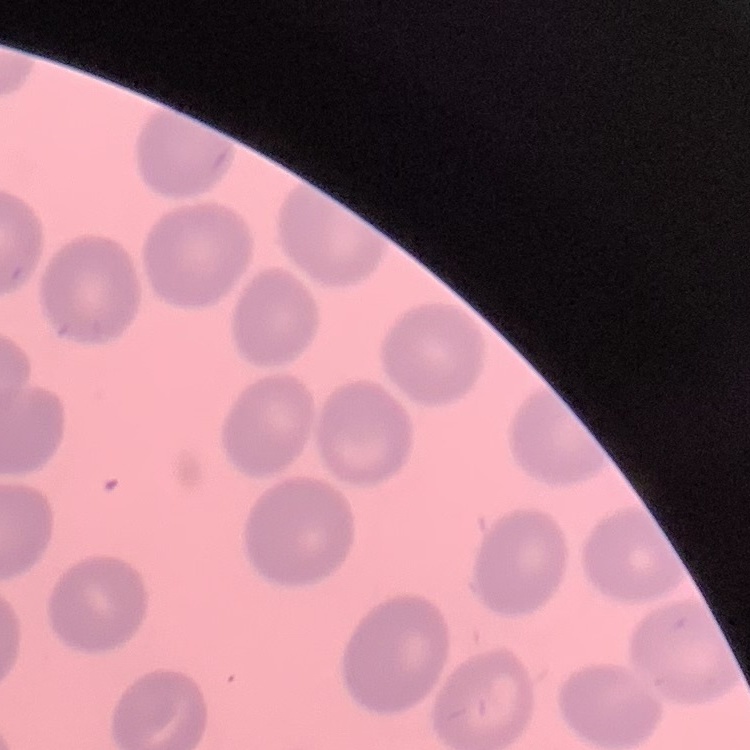
Summary:
  - Erythrocyte morphology: no rouleaux formation
  - Image type: one tile cut from a larger photomicrograph
  - Preparation: thin blood film
  - Stain: Field's or Giemsa